Draw a bounding box around every malaria parasite, every leukocyte, and every artifact (stain precipitate or debris).
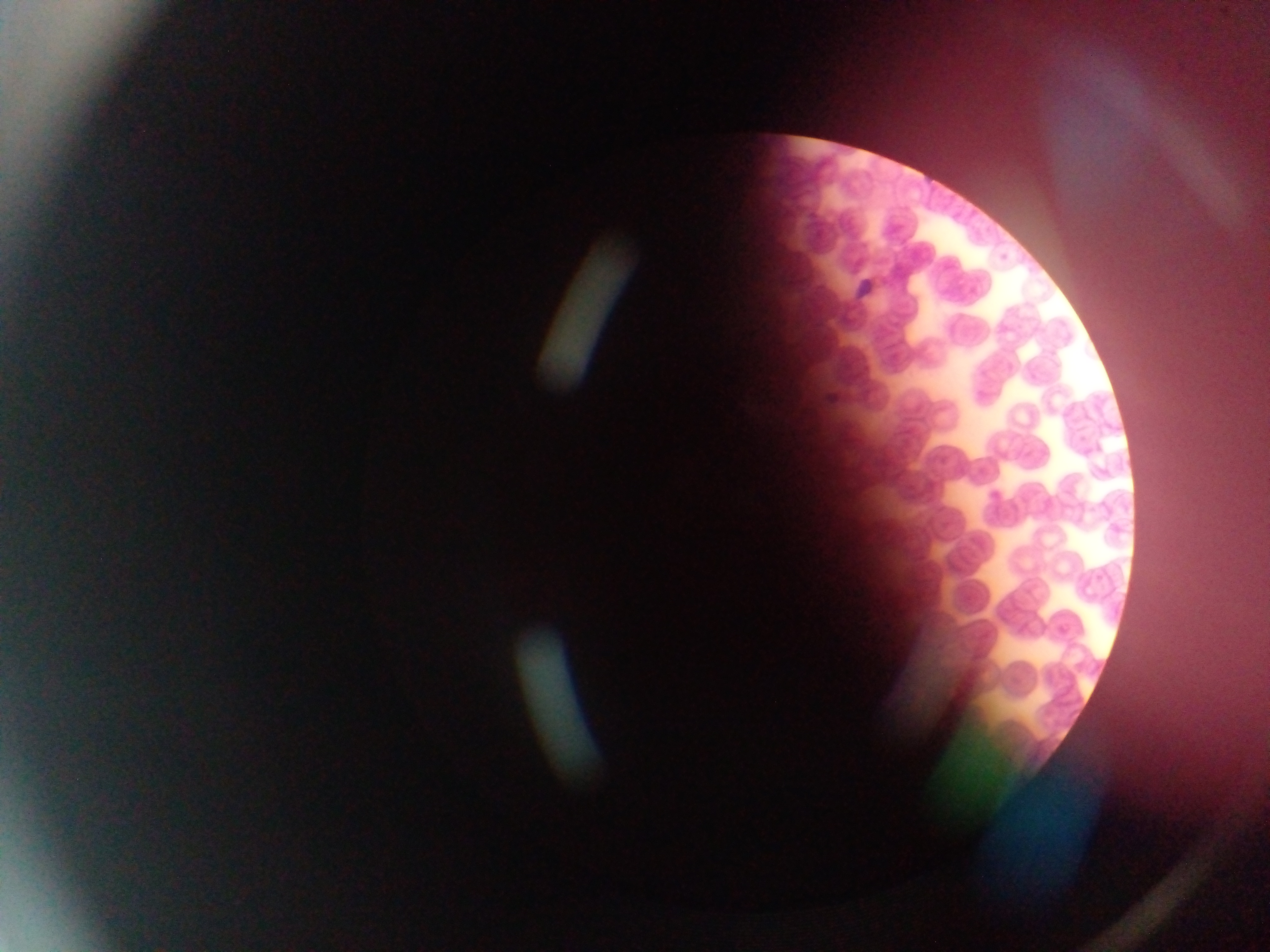

Approximate bounding boxes as {left, top, right, bottom} in pixels.
Malaria parasites: {851, 270, 881, 302}, {822, 365, 853, 405}.
No leukocytes observed.

{
  "field_of_view": "single",
  "capture": "mobile-phone photograph through a microscope",
  "image_size": "1270×952 pixels",
  "preparation": "thin blood smear",
  "country": "Ghana"
}